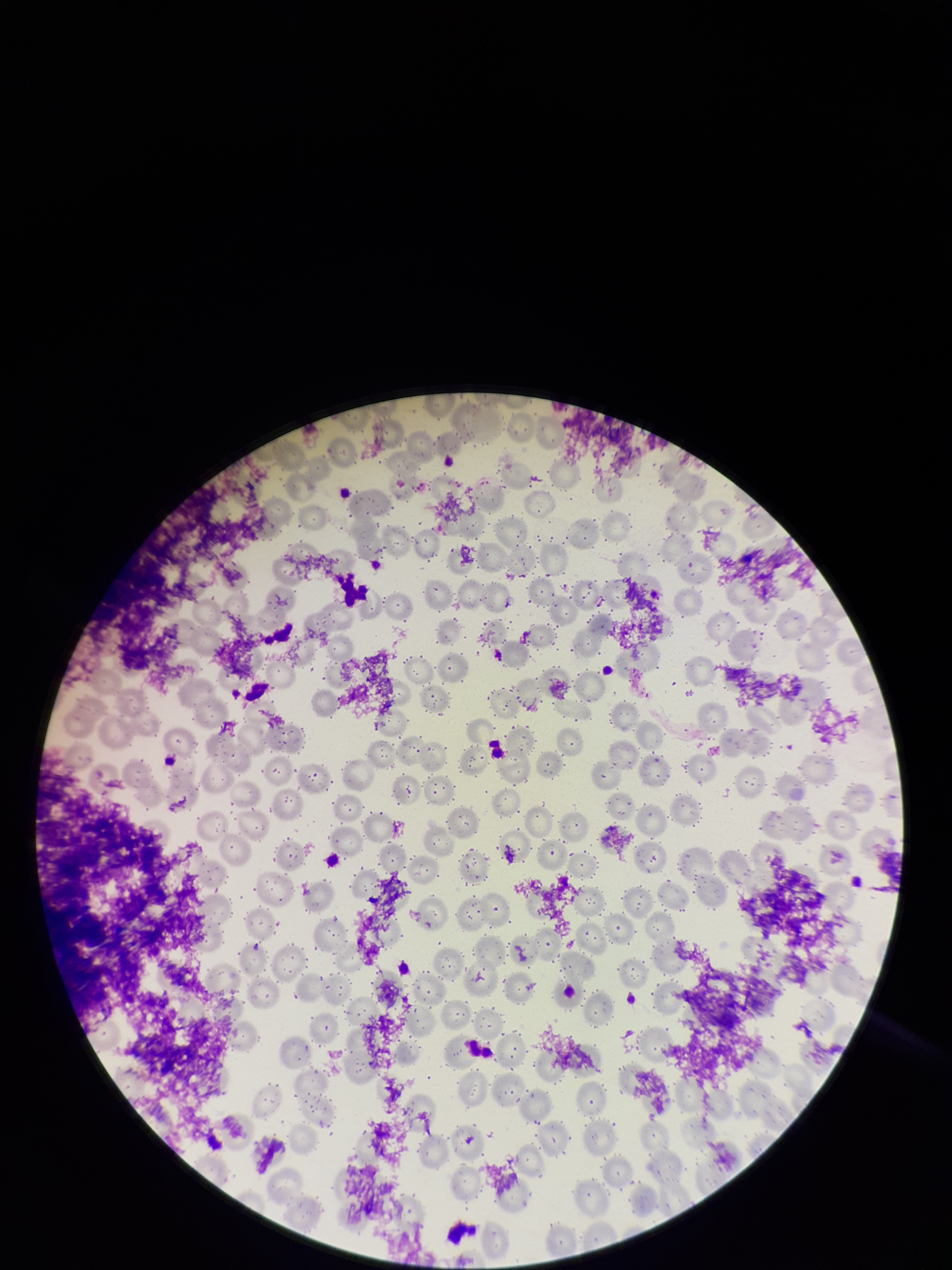

Summary:
  - Red blood cell count: 215
  - Patient malaria status: negative
  - Parasitized red blood cell count: 0
  - Image size: 952×1270 pixels
  - Parasitized red blood cells: none identified
  - Preparation: thin blood smear
  - Stain: Giemsa
  - Capture: smartphone photograph through the microscope eyepiece
  - Field of view: single